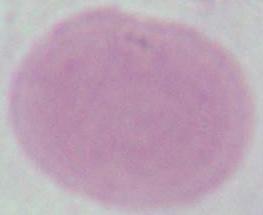

A red blood cell is shown. 1000x magnification. Micrograph.